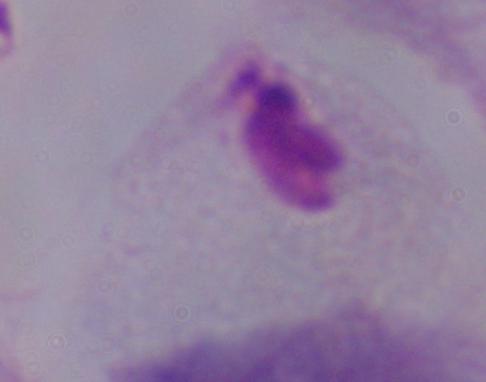
magnification = 1000x
modality = micrograph
identification = trichomonad